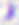

Micrograph. Captured at 400x magnification. Toxoplasma gondii is shown.